Locate and identify every blood parasite.
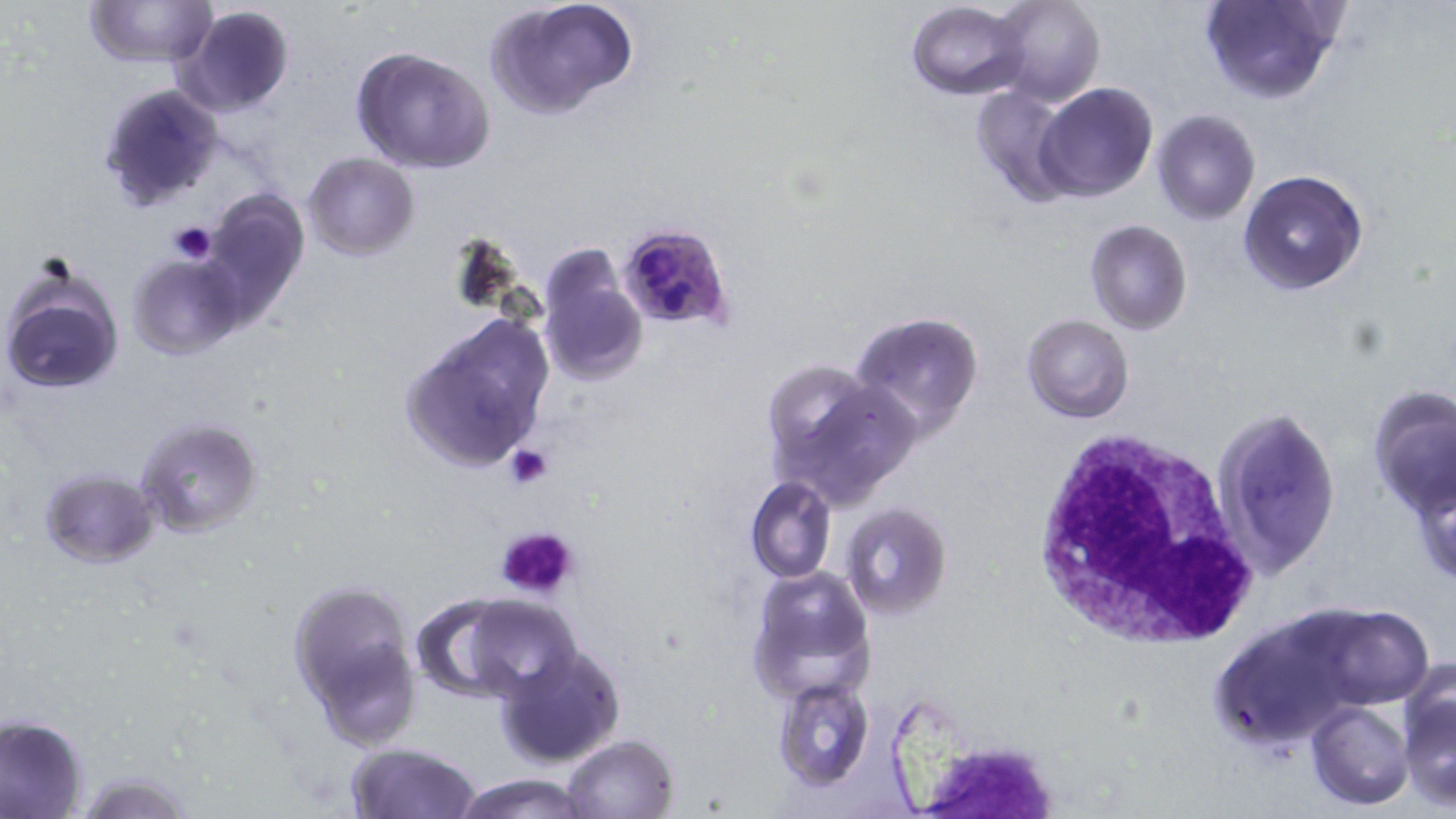

Approximate bounding boxes as [x1, y1, x2, y2] in pixels.
Plasmodium falciparum-infected red blood cells: [618, 222, 736, 332].
No Plasmodium ovale, Plasmodium malariae, Plasmodium vivax, Babesia divergens, or Trypanosoma brucei observed.

Summary:
  - White blood cell locations: [1028, 428, 1259, 650]
  - Platelet locations: [169, 221, 218, 264], [503, 443, 553, 489], [493, 524, 584, 601], [918, 746, 1055, 817]
  - Uninfected red blood cell locations: [83, 0, 218, 68], [485, 0, 640, 118], [987, 0, 1105, 107], [1198, 0, 1343, 105], [906, 2, 1028, 99], [174, 4, 295, 118], [352, 48, 496, 174], [96, 81, 225, 212], [1034, 82, 1158, 201], [970, 84, 1081, 206], [1152, 109, 1261, 225], [303, 152, 419, 260], [1239, 170, 1368, 295], [202, 187, 313, 312], [1083, 219, 1193, 335], [538, 242, 647, 385], [127, 250, 246, 359], [1, 259, 126, 399], [849, 309, 987, 436], [401, 312, 554, 475], [1022, 314, 1135, 423], [761, 364, 918, 505], [1366, 385, 1456, 522], [1213, 405, 1343, 576], [135, 417, 265, 539], [1407, 463, 1456, 590], [40, 467, 159, 567], [746, 477, 838, 583], [841, 503, 952, 619], [745, 565, 875, 703], [288, 576, 421, 743], [410, 594, 527, 702], [461, 596, 585, 700], [1305, 604, 1439, 709], [1207, 611, 1373, 754], [494, 645, 627, 768], [1397, 670, 1456, 809], [772, 676, 875, 790], [1306, 700, 1414, 810], [0, 714, 89, 818], [561, 733, 680, 819], [346, 741, 480, 819], [69, 769, 198, 817], [452, 772, 595, 819]
  - Slide-level diagnosis: Plasmodium falciparum
  - Image size: 1456×819 pixels
  - Field of view: single
  - Preparation: thin blood smear
  - Modality: optical microscopy
  - Magnification: 1000x
  - Stain: May-Grünwald-Giemsa